Identify the parasite.
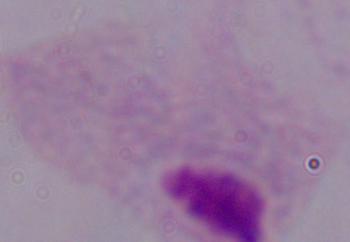

A trichomonad.

Micrograph. 1000x magnification.